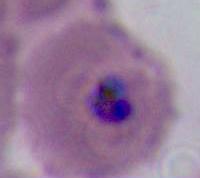
Captured at either 400x or 1000x magnification. A Plasmodium parasite is seen. Micrograph.